Give the extent of all uninfected red blood cells.
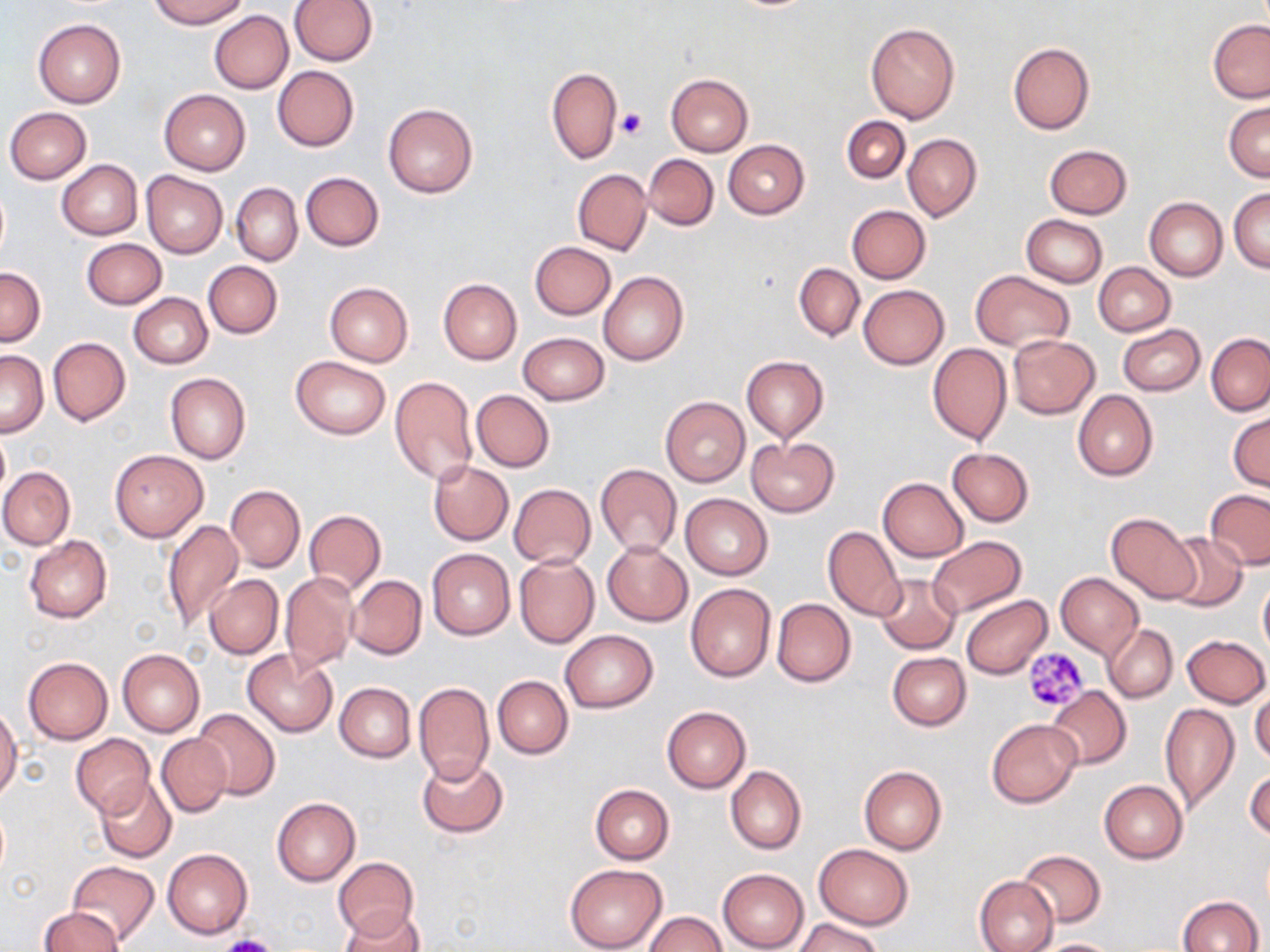

Approximate bounding boxes as (x1, y1, x2, y2) in pixels.
Uninfected red blood cells: (148, 0, 249, 28), (290, 0, 378, 65), (209, 10, 293, 93), (33, 18, 126, 107), (1208, 19, 1270, 102), (865, 22, 961, 124), (1008, 43, 1095, 135), (273, 66, 359, 151), (546, 67, 622, 163), (666, 73, 753, 157), (159, 88, 251, 175), (1224, 100, 1269, 182), (383, 104, 478, 198), (4, 107, 91, 184), (841, 116, 911, 184), (902, 134, 982, 221), (723, 140, 808, 218), (1043, 144, 1133, 219), (643, 153, 718, 229), (56, 159, 142, 239), (573, 169, 652, 254), (141, 171, 229, 257), (301, 172, 384, 251), (232, 183, 302, 265), (1230, 187, 1269, 273), (1145, 198, 1227, 281), (846, 205, 930, 283), (1021, 215, 1107, 286), (81, 239, 166, 310), (530, 242, 616, 320), (203, 260, 283, 338), (1092, 262, 1175, 336), (795, 263, 864, 342), (0, 267, 45, 348), (970, 271, 1073, 352), (598, 272, 688, 366), (438, 278, 522, 365), (325, 282, 412, 366), (858, 285, 948, 370), (129, 292, 212, 369), (1117, 324, 1205, 396), (517, 332, 610, 405), (1206, 333, 1270, 416), (1008, 335, 1100, 419), (48, 337, 131, 425), (927, 342, 1012, 446), (0, 350, 48, 436), (741, 355, 828, 442), (291, 357, 391, 439), (166, 372, 250, 465), (390, 376, 477, 485), (472, 390, 553, 472), (1073, 390, 1157, 480), (660, 397, 749, 487), (1228, 411, 1269, 492), (0, 428, 10, 502), (747, 436, 839, 517), (946, 447, 1033, 526), (109, 449, 208, 542), (429, 461, 514, 545), (595, 463, 682, 557), (0, 467, 74, 549), (878, 477, 968, 561), (509, 483, 596, 568), (226, 485, 305, 571), (1204, 489, 1270, 569), (680, 493, 773, 580), (304, 509, 386, 595), (1106, 513, 1200, 604), (163, 519, 245, 631), (824, 526, 904, 620), (1163, 531, 1246, 609), (24, 535, 112, 623), (926, 536, 1027, 619), (602, 540, 692, 627), (427, 549, 515, 640), (514, 555, 599, 648), (281, 573, 358, 672), (1055, 573, 1143, 657), (205, 575, 283, 659), (348, 575, 427, 660), (875, 575, 960, 654), (1258, 578, 1270, 661), (685, 583, 776, 681), (961, 595, 1053, 679), (772, 598, 855, 687), (1103, 624, 1178, 703), (559, 629, 658, 713), (1183, 634, 1269, 706), (117, 649, 205, 736), (243, 649, 337, 737), (887, 652, 971, 731), (23, 656, 112, 744), (493, 676, 573, 759), (334, 682, 416, 762), (414, 682, 495, 783), (1046, 686, 1131, 769), (1250, 687, 1270, 764), (1159, 702, 1239, 814), (0, 705, 22, 802), (190, 706, 279, 801), (661, 706, 752, 793), (987, 718, 1081, 807), (157, 733, 231, 816), (71, 734, 155, 816), (416, 756, 507, 837), (1245, 764, 1270, 843), (726, 765, 806, 854), (859, 765, 947, 854), (95, 777, 177, 862), (1099, 780, 1188, 864), (590, 784, 674, 864), (272, 797, 360, 885), (813, 844, 913, 929), (162, 848, 253, 938), (1017, 849, 1106, 927), (332, 858, 420, 941), (68, 861, 159, 943), (563, 864, 668, 952), (718, 869, 809, 951), (974, 875, 1059, 952), (1177, 895, 1264, 952), (38, 906, 123, 952), (340, 907, 426, 952), (645, 912, 726, 952), (795, 917, 883, 952), (1032, 938, 1120, 952).

Summary:
  - Platelet locations: (618, 108, 647, 139), (1024, 646, 1091, 712), (215, 936, 280, 952)
  - Slide-level diagnosis: negative for blood parasites
  - Field of view: one of a larger specimen
  - Preparation: thin blood film
  - Image size: 1270×952 pixels
  - Magnification: 1000x
  - Modality: optical microscopy
  - Stain: May-Grünwald-Giemsa